Locate every Plasmodium ovale-infected red blood cell.
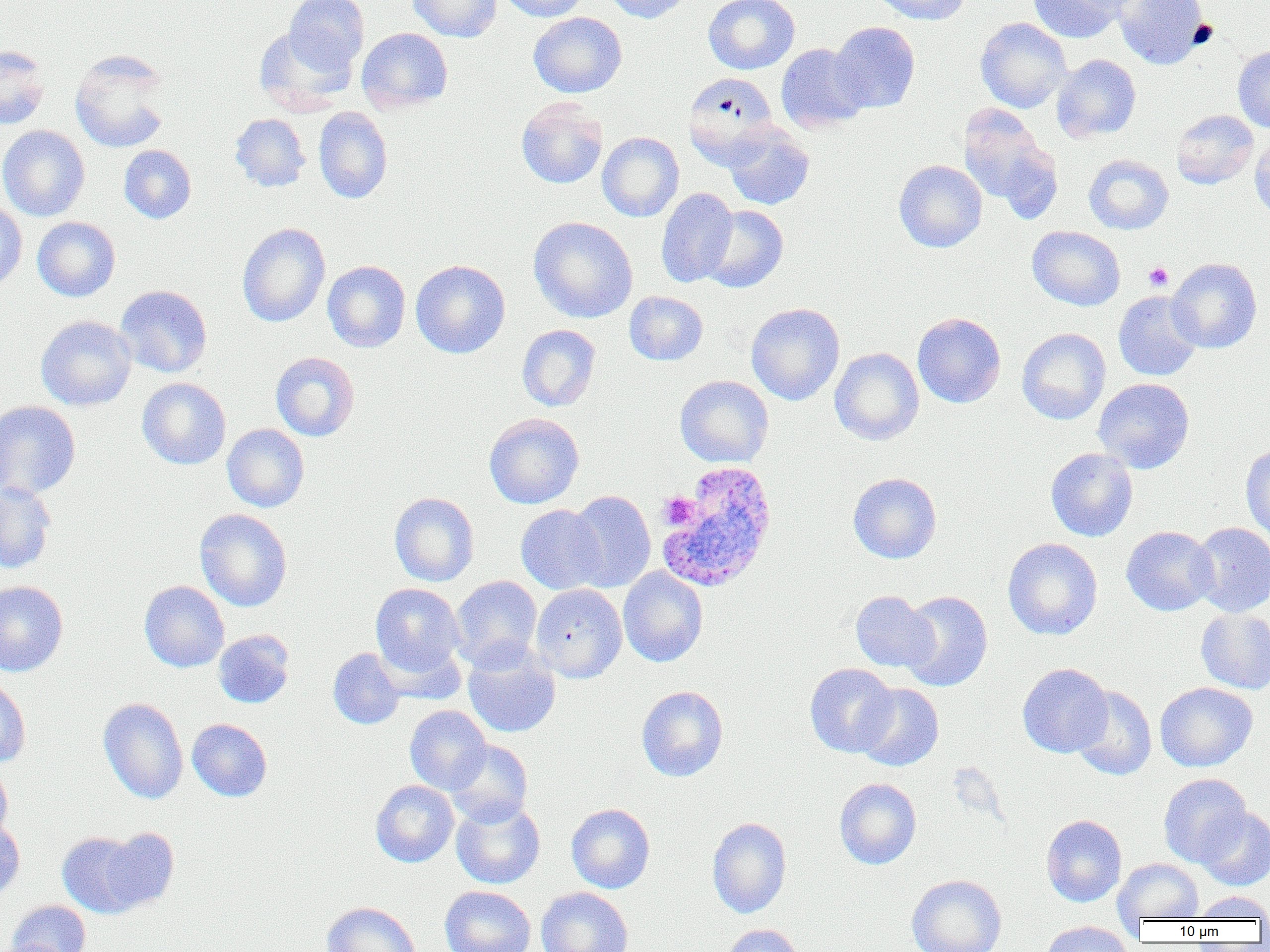

Approximate bounding boxes as [x1, y1, x2, y2] in pixels.
Plasmodium ovale-infected red blood cells: [656, 461, 778, 594].

Platelet locations: [1144, 262, 1173, 291], [658, 493, 700, 530]. Uninfected red blood cell locations: [284, 0, 369, 74], [408, 0, 502, 42], [498, 0, 588, 21], [601, 0, 693, 23], [703, 0, 800, 74], [870, 0, 970, 26], [1027, 0, 1128, 43], [1113, 0, 1210, 69], [528, 12, 627, 98], [975, 17, 1072, 113], [830, 22, 920, 113], [253, 26, 356, 115], [356, 28, 453, 113], [776, 43, 869, 132], [0, 45, 50, 130], [1233, 45, 1270, 133], [69, 49, 172, 153], [1052, 54, 1141, 142], [683, 72, 779, 166], [516, 97, 608, 189], [957, 105, 1059, 216], [313, 106, 393, 204], [1171, 110, 1258, 189], [230, 113, 310, 192], [722, 124, 815, 210], [0, 125, 90, 221], [597, 132, 684, 222], [1250, 138, 1270, 225], [119, 145, 196, 224], [1083, 154, 1173, 234], [893, 160, 987, 253], [656, 187, 738, 288], [0, 201, 27, 291], [701, 205, 789, 293], [32, 216, 120, 302], [528, 216, 638, 323], [237, 223, 330, 328], [1027, 226, 1126, 311], [1167, 258, 1262, 353], [410, 259, 510, 358], [322, 260, 410, 352], [115, 285, 212, 378], [624, 291, 708, 366], [1113, 291, 1203, 381], [745, 302, 845, 405], [912, 312, 1006, 408], [36, 315, 136, 411], [517, 324, 601, 411], [1017, 328, 1111, 425], [829, 348, 924, 445], [271, 352, 359, 441], [675, 375, 774, 468], [137, 377, 231, 470], [1093, 378, 1194, 473], [0, 401, 81, 500], [484, 412, 584, 509], [222, 423, 309, 512], [1240, 443, 1270, 542], [1045, 448, 1138, 542], [848, 472, 942, 563], [0, 482, 56, 574], [567, 491, 655, 592], [389, 492, 479, 586], [516, 504, 606, 594], [194, 508, 292, 611], [1190, 522, 1270, 617], [1121, 526, 1219, 616], [1003, 538, 1102, 640], [618, 566, 709, 667], [450, 575, 542, 670], [0, 580, 68, 676], [139, 581, 229, 672], [370, 583, 466, 678], [531, 584, 627, 682], [850, 590, 937, 671], [899, 590, 993, 692], [1196, 608, 1270, 694], [213, 630, 295, 709], [375, 638, 465, 704], [463, 643, 561, 738], [328, 647, 405, 729], [804, 663, 899, 757], [1017, 663, 1113, 758], [0, 678, 31, 767], [1155, 682, 1257, 772], [854, 683, 943, 771], [1071, 685, 1157, 780], [636, 686, 728, 782], [98, 698, 188, 803], [405, 705, 492, 794], [187, 719, 272, 801], [445, 739, 533, 827], [0, 764, 12, 843], [1158, 773, 1251, 867], [834, 778, 921, 869], [370, 780, 459, 867], [451, 799, 545, 889], [566, 803, 655, 893], [1196, 808, 1270, 890], [1041, 815, 1127, 906], [707, 817, 792, 918], [0, 818, 25, 901], [99, 827, 179, 913], [57, 832, 145, 918], [1113, 858, 1204, 923], [906, 874, 1007, 952], [440, 886, 536, 952], [536, 887, 633, 952], [1192, 891, 1270, 921], [6, 900, 90, 952], [321, 901, 420, 952], [1040, 921, 1133, 952], [721, 924, 804, 952]. Slide-level diagnosis: Plasmodium ovale. Image is 1270×952 pixels. Thin blood film. Optical microscopy. One field of a larger specimen. 1000x magnification.